Report the malaria status of this cell.
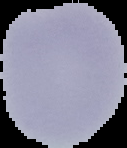

It is uninfected.

preparation = thin blood film
image type = segmented cell region on a black background
image size = 127×148 pixels